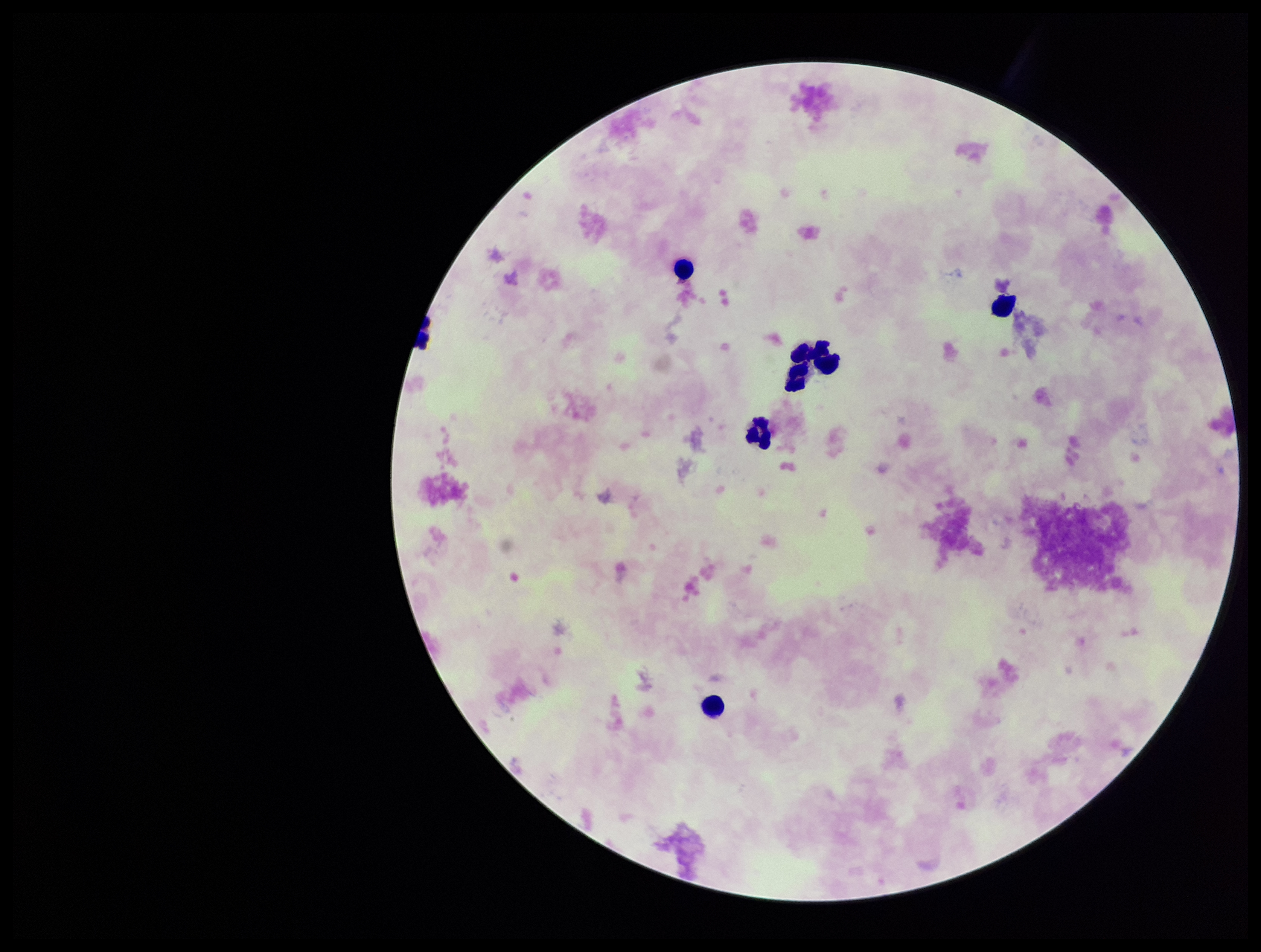
{
  "field_of_view": "single",
  "preparation": "thick blood smear",
  "image_size": "1261×952 pixels",
  "stain": "Giemsa",
  "leukocyte_count": 6,
  "parasite_count": 0,
  "plasmodium_parasites": "none detected",
  "capture": "smartphone photograph through the microscope eyepiece",
  "patient_malaria_status": "negative"
}